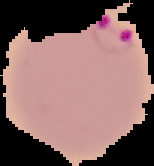

Summary:
  - Image type: segmented cell region on a black background
  - Preparation: thin blood smear
  - Malaria status: parasitized
  - Image size: 154×166 pixels